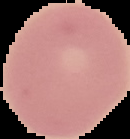

Cell region segmented out of the field of view; the surrounding area is masked to black. Result: no malaria parasites detected. From a thin blood smear. Image is 130×139 pixels.